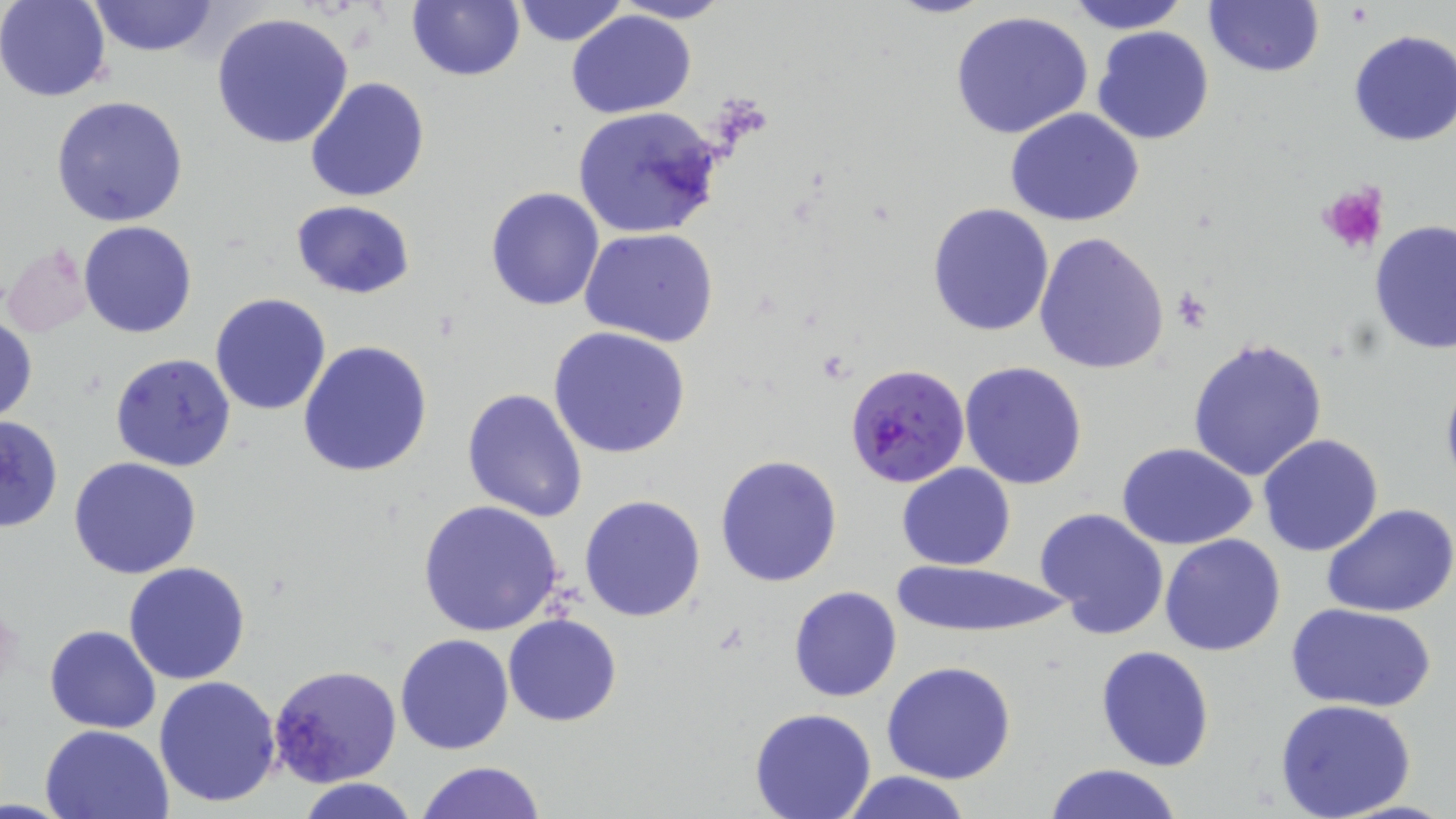 Approximate bounding boxes as [x1, y1, x2, y2] in pixels. Platelet locations: [1317, 182, 1389, 255], [1168, 291, 1214, 330]. Plasmodium falciparum-infected red blood cell locations: [844, 361, 971, 489]. Uninfected red blood cell locations: [0, 0, 111, 101], [88, 0, 220, 57], [408, 0, 524, 82], [509, 0, 628, 47], [1064, 0, 1191, 33], [1203, 0, 1325, 79], [610, 1, 733, 24], [210, 10, 355, 150], [567, 10, 696, 118], [949, 10, 1096, 141], [1092, 26, 1215, 147], [1347, 29, 1456, 146], [304, 76, 431, 204], [51, 95, 189, 228], [573, 106, 726, 239], [1005, 107, 1145, 228], [485, 186, 606, 311], [290, 200, 415, 300], [927, 202, 1055, 337], [79, 220, 197, 338], [1369, 220, 1456, 355], [580, 227, 719, 348], [1033, 233, 1172, 376], [3, 242, 95, 336], [210, 293, 331, 416], [0, 312, 37, 424], [547, 326, 692, 459], [1187, 338, 1328, 481], [297, 340, 432, 478], [110, 352, 238, 474], [959, 360, 1089, 490], [1439, 367, 1456, 496], [461, 387, 587, 524], [0, 413, 63, 533], [1258, 434, 1384, 556], [1118, 443, 1258, 549], [714, 454, 844, 588], [68, 457, 202, 579], [897, 463, 1016, 569], [579, 495, 706, 623], [416, 499, 565, 637], [1323, 502, 1456, 617], [1037, 506, 1169, 640], [1159, 533, 1287, 657], [890, 559, 1069, 635], [123, 561, 251, 684], [789, 586, 902, 702], [1290, 603, 1435, 713], [503, 612, 623, 727], [44, 625, 161, 733], [394, 633, 515, 754], [1095, 644, 1215, 772], [881, 661, 1016, 785], [269, 663, 402, 787], [153, 675, 282, 809], [1275, 698, 1419, 819], [749, 709, 875, 819], [40, 723, 173, 819], [416, 760, 546, 818], [1041, 763, 1187, 819], [836, 771, 976, 819], [296, 777, 420, 819]. Slide-level diagnosis: Plasmodium falciparum. May-Grünwald-Giemsa-stained preparation. One field of a larger specimen. Light microscopy. Image is 1456×819 pixels. Thin blood smear. 1000x magnification.